Classify this cell by malaria status.
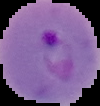
Parasitized.

From a thin blood film. Image is 100×106 pixels. Cell region segmented out of the field of view; the surrounding area is masked to black.